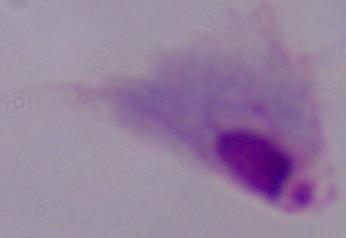
Summary:
  - Modality: photomicrograph
  - Identification: trichomonad
  - Magnification: 1000x